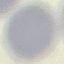
Malaria status: uninfected. Acquired by smartphone through the microscope eyepiece. Thin blood smear. Giemsa-stained preparation. Automatically extracted cell patch, resized to 64 × 64 pixels.